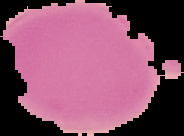
preparation = thin blood smear
image type = segmented cell region with the area outside set to black
image size = 184×136 pixels
malaria status = uninfected